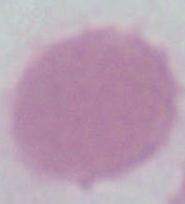

Summary:
  - Identification: erythrocyte
  - Modality: micrograph
  - Magnification: 1000x